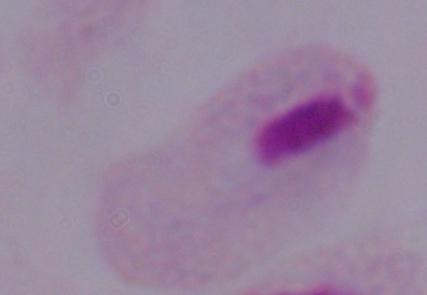
Summary:
  - Modality: micrograph
  - Magnification: 1000x
  - Identification: trichomonad